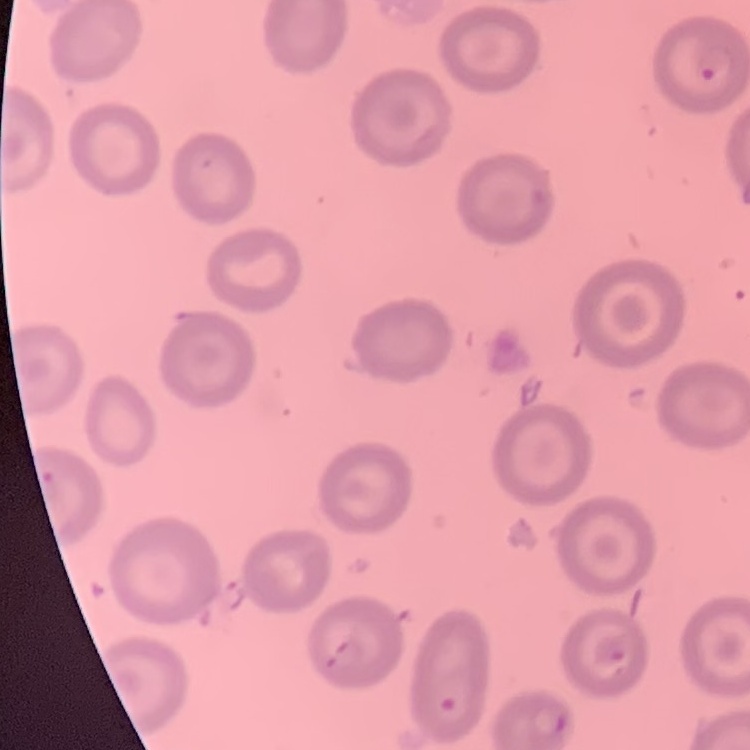
red blood cell morphology = no rouleaux formation
image type = one tile cut from a larger photomicrograph
preparation = thin peripheral smear
stain = Field's or Giemsa